State which parasite is depicted.
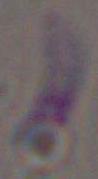
This is Toxoplasma gondii.

modality: micrograph
magnification: 1000x